Report the malaria status of this cell.
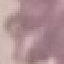
It is uninfected.

Photographed with a smartphone camera at the microscope eyepiece. Automatically extracted cell patch, resized to 64 × 64 pixels. Thin blood film. Giemsa-stained preparation.